Locate every leukocyte (white blood cell).
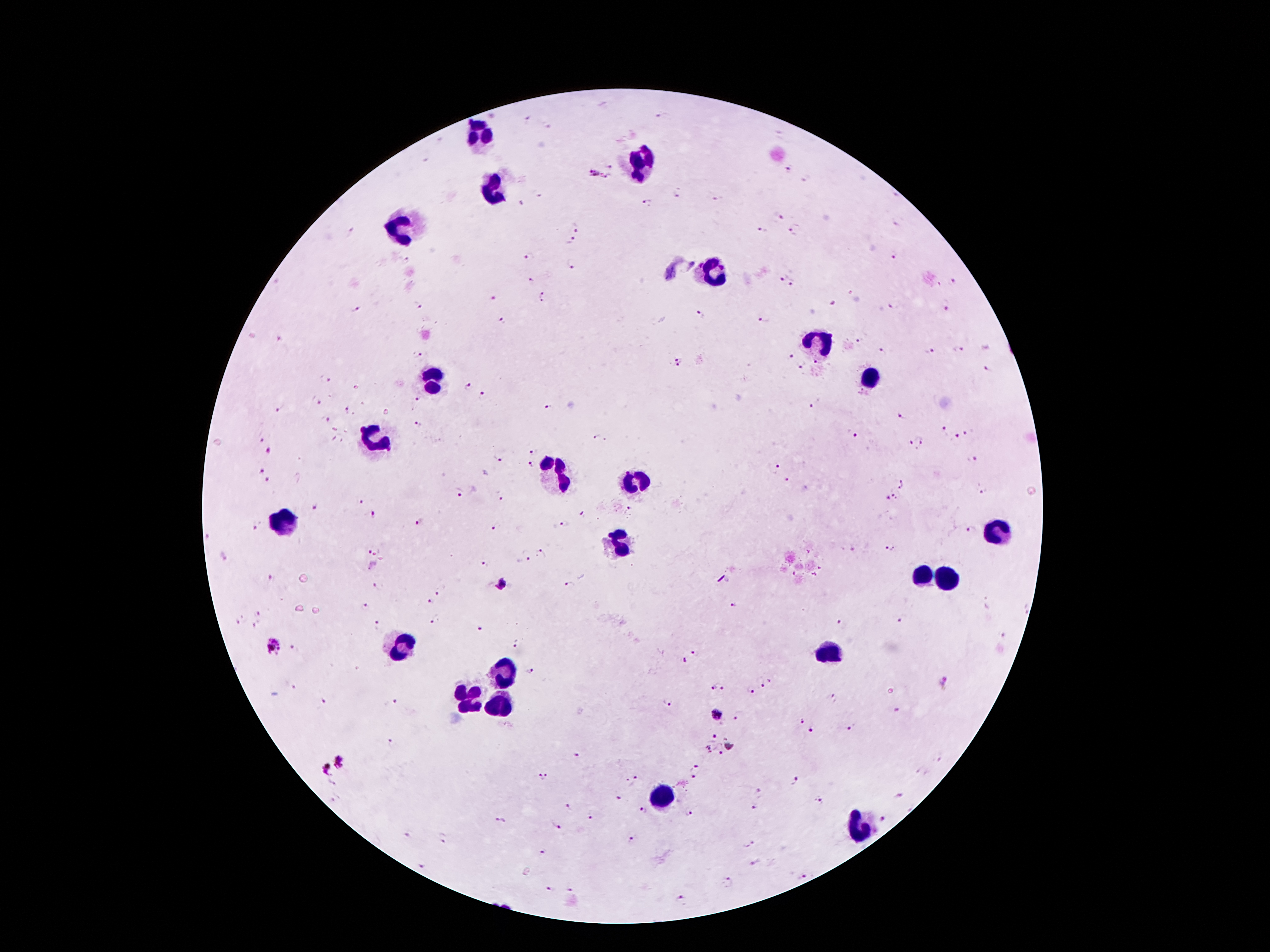
Approximate centers as [x, y] in pixels.
Leukocytes: [479, 134], [640, 166], [490, 185], [404, 229], [714, 272], [819, 341], [869, 379], [434, 381], [375, 443], [554, 476], [636, 483], [283, 522], [1002, 532], [621, 545], [921, 576], [949, 580], [403, 644], [830, 652], [501, 672], [472, 701], [498, 701], [664, 797], [862, 826].

Plasmodium parasite locations: [527, 118], [548, 124], [609, 165], [789, 168], [593, 173], [611, 178], [804, 178], [675, 193], [538, 195], [718, 198], [649, 202], [521, 204], [779, 217], [577, 226], [763, 230], [794, 234], [571, 240], [894, 255], [406, 260], [573, 264], [670, 273], [782, 276], [532, 280], [952, 282], [792, 284], [539, 294], [492, 299], [542, 301], [835, 303], [893, 305], [416, 306], [947, 308], [353, 310], [700, 314], [765, 320], [503, 321], [861, 340], [957, 348], [929, 351], [883, 352], [789, 355], [416, 356], [815, 363], [678, 364], [802, 366], [987, 371], [327, 378], [466, 385], [863, 391], [483, 395], [416, 399], [314, 401], [815, 403], [547, 404], [277, 409], [346, 410], [386, 412], [900, 415], [325, 421], [417, 424], [944, 431], [966, 432], [852, 434], [958, 436], [596, 437], [261, 440], [923, 440], [914, 447], [269, 451], [534, 452], [496, 457], [974, 460], [533, 464], [776, 466], [262, 471], [267, 480], [787, 480], [904, 484], [983, 490], [459, 494], [897, 494], [499, 496], [887, 499], [360, 501], [313, 507], [631, 510], [582, 514], [372, 515], [419, 521], [564, 524], [254, 525], [495, 527], [971, 528], [891, 549], [365, 551], [542, 553], [526, 556], [224, 558], [486, 563], [272, 579], [569, 584], [374, 585], [439, 590], [429, 603], [733, 603], [365, 605], [257, 612], [239, 620], [434, 620], [903, 620], [841, 623], [258, 625], [377, 625], [480, 628], [514, 644], [272, 647], [294, 649], [695, 652], [685, 658], [531, 672], [761, 679], [947, 683], [294, 687], [719, 688], [749, 692], [835, 698], [325, 700], [391, 701], [667, 704], [896, 709], [717, 714], [739, 714], [802, 721], [851, 727], [810, 730], [714, 736], [392, 744], [707, 748], [722, 752], [575, 755], [342, 762], [697, 768], [324, 769], [542, 777], [696, 777], [636, 779], [795, 780], [628, 782], [759, 793], [900, 795], [620, 798], [334, 801], [818, 802], [567, 807], [753, 809], [642, 810], [689, 812], [589, 815], [883, 818], [499, 821], [556, 826], [408, 834], [632, 837], [443, 838], [749, 844], [543, 851], [755, 864], [422, 866], [802, 876], [727, 883], [548, 889], [569, 890], [680, 898]. Patient malaria status: positive for Plasmodium falciparum. 100x magnification. Photographed through the microscope eyepiece with a smartphone camera. One field from this slide. Giemsa-stained preparation. Thick blood film. Image is 1270×952 pixels.